Outline each blood parasite and name the species.
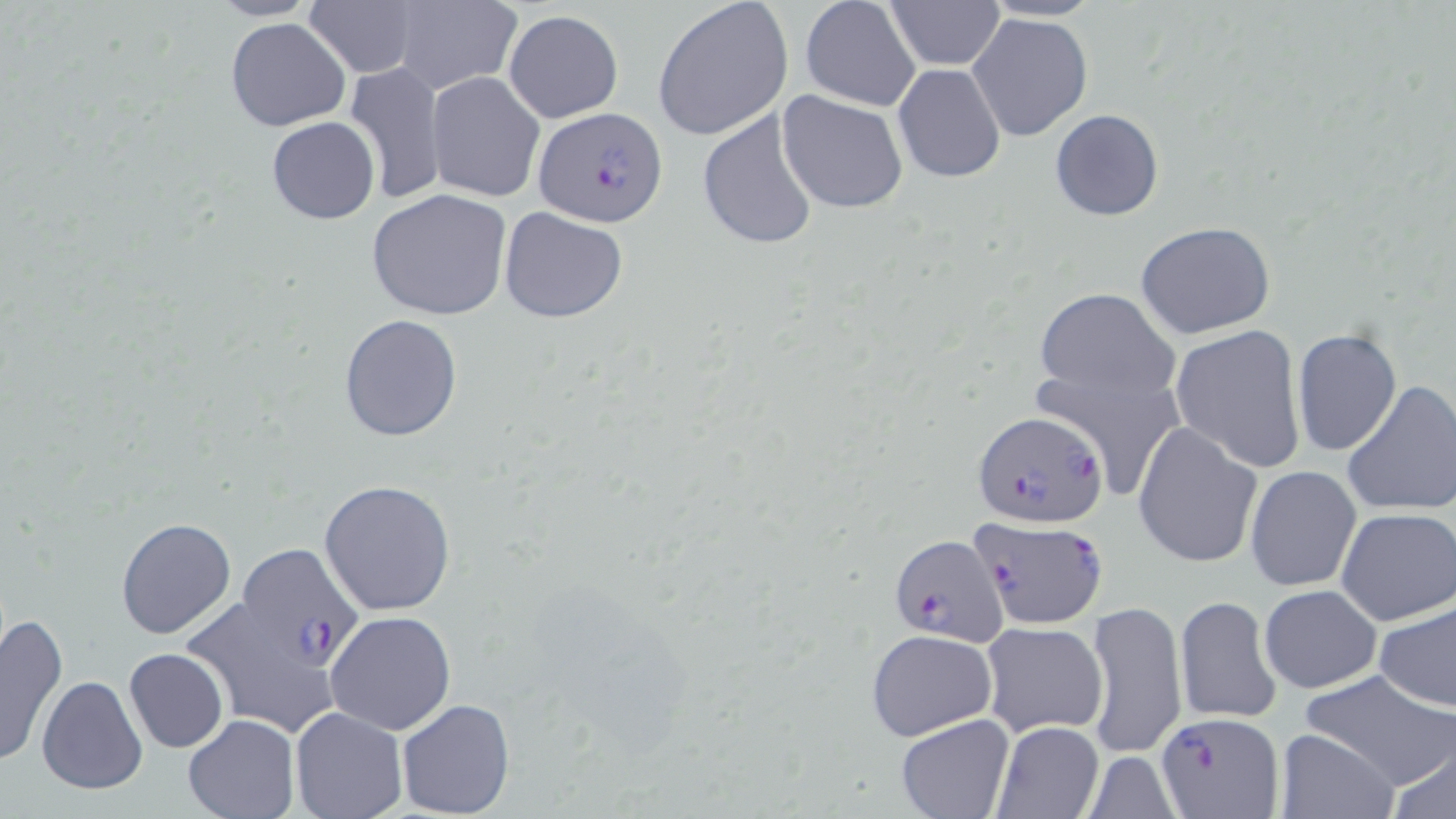

Approximate bounding boxes as named x1/y1/x2/y2 corners in pixels.
Plasmodium falciparum-infected red blood cells: (x1=533, y1=107, x2=667, y2=227), (x1=974, y1=412, x2=1108, y2=528), (x1=969, y1=517, x2=1108, y2=632), (x1=886, y1=534, x2=1007, y2=645), (x1=236, y1=541, x2=363, y2=669), (x1=1154, y1=711, x2=1285, y2=816).
No Plasmodium ovale, Plasmodium malariae, Plasmodium vivax, Babesia divergens, or Trypanosoma brucei observed.

Uninfected red blood cell locations: (x1=652, y1=0, x2=792, y2=142), (x1=799, y1=0, x2=923, y2=111), (x1=207, y1=1, x2=319, y2=22), (x1=302, y1=1, x2=420, y2=79), (x1=388, y1=1, x2=523, y2=93), (x1=883, y1=1, x2=1004, y2=70), (x1=981, y1=1, x2=1102, y2=23), (x1=504, y1=10, x2=623, y2=124), (x1=966, y1=12, x2=1094, y2=142), (x1=225, y1=18, x2=352, y2=133), (x1=343, y1=62, x2=448, y2=205), (x1=894, y1=63, x2=1006, y2=183), (x1=425, y1=72, x2=544, y2=202), (x1=776, y1=90, x2=909, y2=214), (x1=696, y1=106, x2=822, y2=251), (x1=1050, y1=109, x2=1164, y2=222), (x1=266, y1=117, x2=380, y2=225), (x1=366, y1=189, x2=513, y2=323), (x1=497, y1=206, x2=628, y2=322), (x1=1135, y1=221, x2=1276, y2=340), (x1=1032, y1=287, x2=1179, y2=406), (x1=338, y1=312, x2=464, y2=443), (x1=1170, y1=323, x2=1307, y2=473), (x1=1291, y1=329, x2=1401, y2=457), (x1=1030, y1=364, x2=1185, y2=501), (x1=1341, y1=379, x2=1456, y2=517), (x1=1132, y1=420, x2=1263, y2=569), (x1=1245, y1=467, x2=1361, y2=592), (x1=319, y1=478, x2=457, y2=615), (x1=1335, y1=508, x2=1454, y2=626), (x1=115, y1=518, x2=237, y2=639), (x1=1258, y1=584, x2=1382, y2=694), (x1=1176, y1=595, x2=1280, y2=724), (x1=1374, y1=597, x2=1456, y2=714), (x1=1086, y1=598, x2=1187, y2=760), (x1=325, y1=610, x2=457, y2=736), (x1=0, y1=612, x2=68, y2=766), (x1=979, y1=621, x2=1109, y2=738), (x1=865, y1=629, x2=997, y2=741), (x1=123, y1=648, x2=229, y2=753), (x1=1296, y1=668, x2=1455, y2=790), (x1=36, y1=675, x2=147, y2=795), (x1=396, y1=698, x2=516, y2=819), (x1=291, y1=708, x2=408, y2=819), (x1=895, y1=713, x2=1014, y2=818), (x1=184, y1=714, x2=300, y2=819), (x1=991, y1=722, x2=1104, y2=818), (x1=1276, y1=729, x2=1397, y2=819), (x1=1384, y1=745, x2=1456, y2=819), (x1=1080, y1=750, x2=1185, y2=818). Slide-level diagnosis: Plasmodium falciparum. One field of a larger specimen. May-Grünwald-Giemsa-stained preparation. Light microscopy. Thin blood film. Image is 1456×819 pixels. Captured at 1000x magnification.